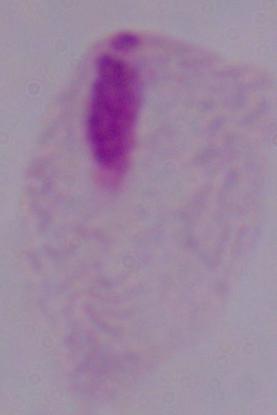

{
  "magnification": "1000x",
  "modality": "micrograph",
  "identification": "trichomonad"
}